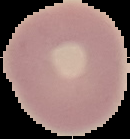
malaria_status: uninfected
preparation: thin blood film
image_type: segmented cell region with the area outside set to black
image_size: 130×139 pixels